Locate every leukocyte (white blood cell).
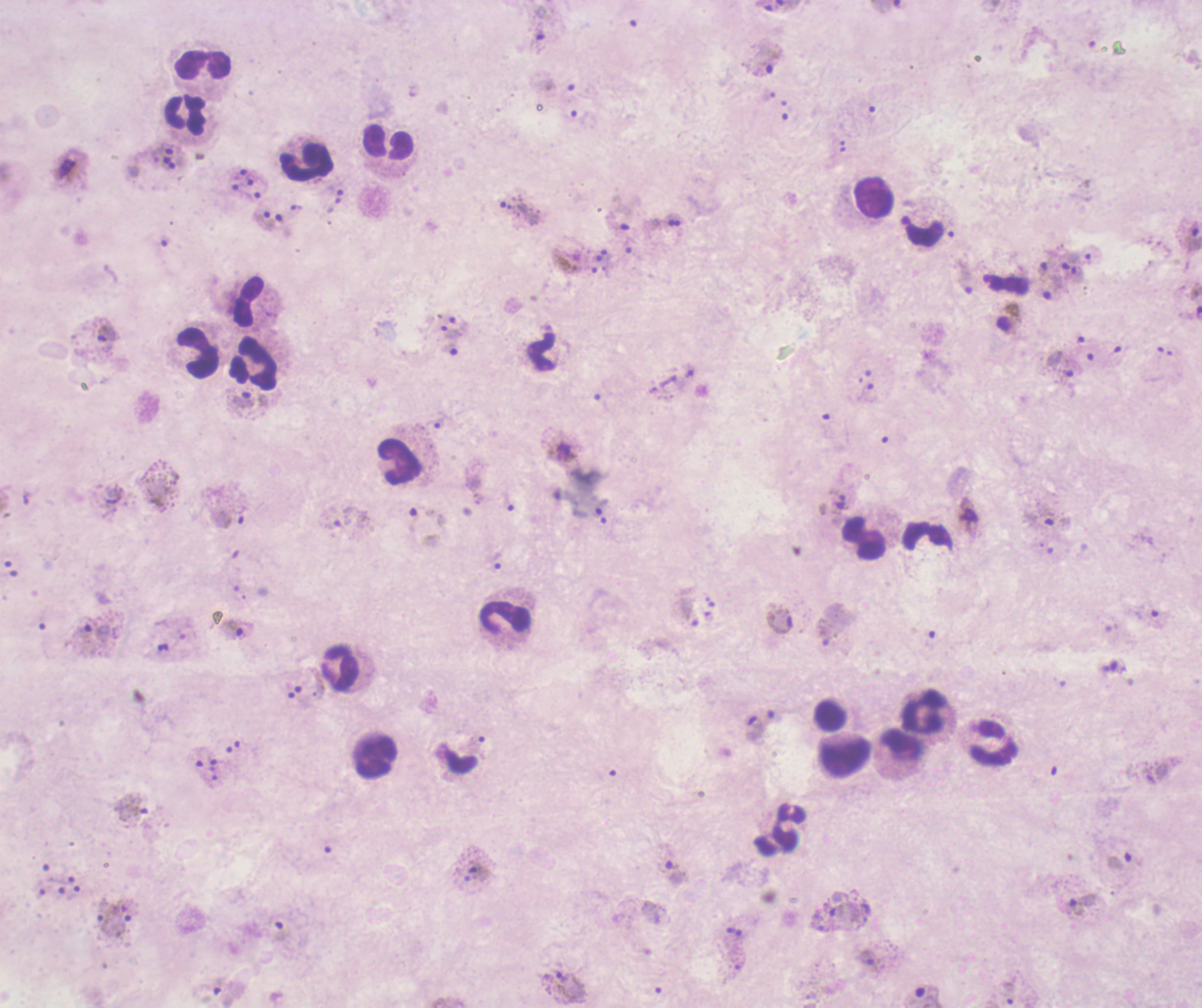
Approximate centers as {x, y} in pixels.
Leukocytes: {202, 66}, {185, 113}, {388, 144}, {306, 161}, {872, 198}, {923, 231}, {248, 303}, {542, 352}, {196, 355}, {254, 363}, {396, 462}, {927, 535}, {864, 541}, {505, 618}, {340, 671}, {922, 710}, {995, 744}, {902, 746}, {373, 757}, {845, 757}, {778, 830}.

Approximate centers as {x, y} in pixels.
Summary:
  - Trophozoite locations: {539, 39}, {765, 58}, {240, 192}, {260, 215}, {1191, 235}, {1042, 268}, {1078, 276}, {966, 278}, {1048, 290}, {451, 332}, {107, 336}, {248, 404}, {1049, 520}, {495, 560}, {779, 620}, {236, 630}, {83, 636}, {1157, 773}, {133, 810}, {1118, 859}, {479, 868}, {674, 871}, {1083, 904}, {563, 978}, {927, 996}
  - Gametocyte locations: {68, 168}, {562, 451}, {968, 519}
  - Life-cycle stages observed: trophozoite, gametocyte
  - Stain: Romanowsky
  - Field of view: single
  - Preparation: thick smear of blood
  - Magnification: 100x
  - Image size: 1202×1008 pixels
  - Coloration quality: bad
  - Context: previously used in a real diagnosis
  - Background quality: unsatisfactory
  - Result: positive for Plasmodium parasites